Identify the blood parasite species.
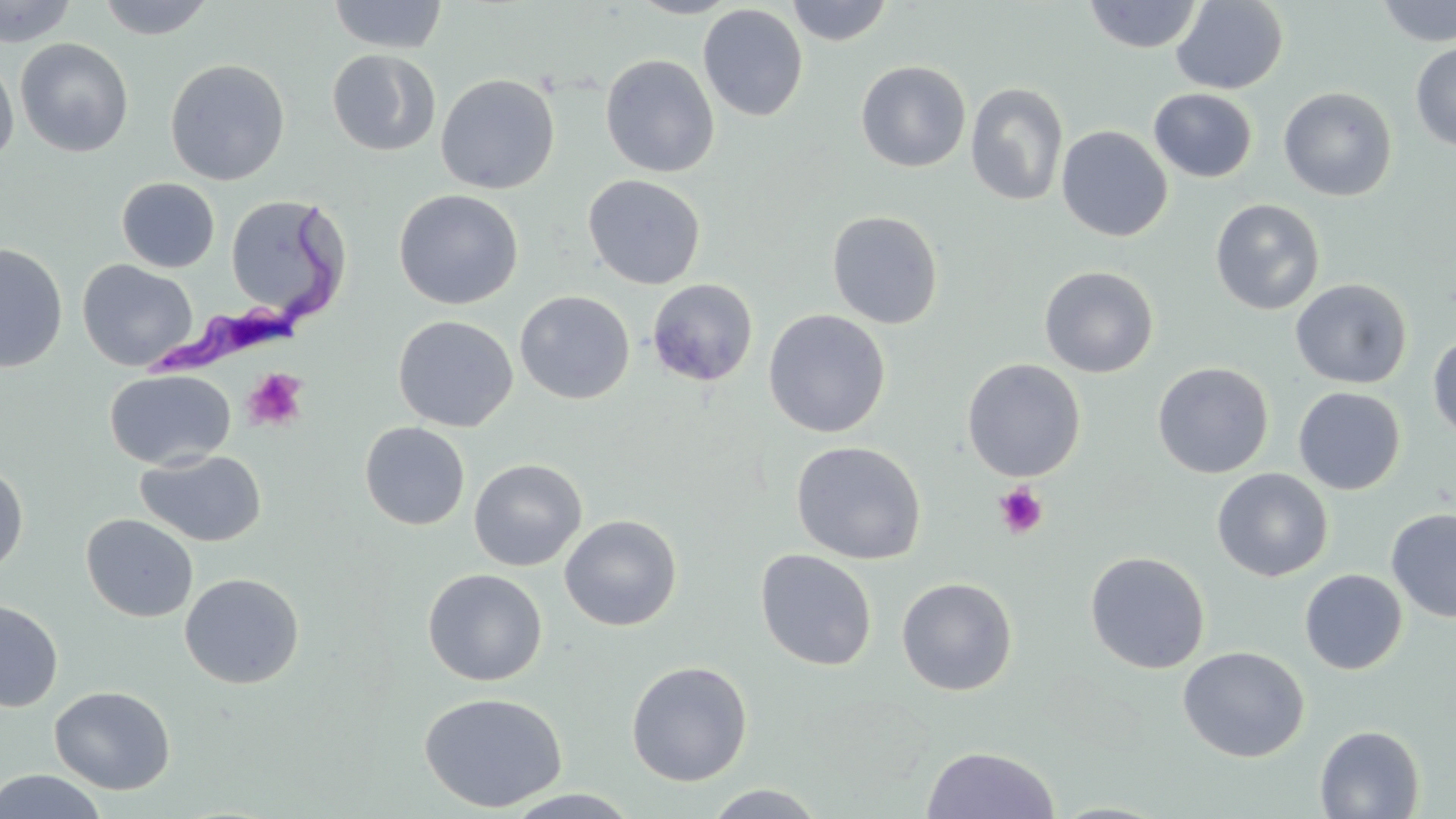
Trypanosoma brucei.

image size = 1456×819 pixels
platelet locations = approximate bounding boxes as named x1/y1/x2/y2 corners in pixels: (x1=241, y1=367, x2=309, y2=433), (x1=993, y1=483, x2=1049, y2=538)
stain = May-Grünwald-Giemsa
modality = optical microscopy
preparation = thin blood smear
magnification = 1000x
uninfected red blood cell locations = approximate bounding boxes as named x1/y1/x2/y2 corners in pixels: (x1=95, y1=0, x2=216, y2=40), (x1=328, y1=0, x2=448, y2=54), (x1=627, y1=0, x2=742, y2=19), (x1=785, y1=0, x2=894, y2=46), (x1=0, y1=1, x2=78, y2=47), (x1=1082, y1=1, x2=1204, y2=53), (x1=1170, y1=1, x2=1289, y2=94), (x1=1376, y1=1, x2=1456, y2=46), (x1=697, y1=4, x2=808, y2=122), (x1=16, y1=38, x2=134, y2=158), (x1=1410, y1=42, x2=1456, y2=153), (x1=326, y1=49, x2=441, y2=157), (x1=0, y1=52, x2=19, y2=165), (x1=600, y1=54, x2=720, y2=178), (x1=165, y1=58, x2=290, y2=186), (x1=856, y1=60, x2=971, y2=172), (x1=435, y1=73, x2=560, y2=194), (x1=965, y1=82, x2=1069, y2=207), (x1=1278, y1=86, x2=1397, y2=201), (x1=1149, y1=88, x2=1258, y2=183), (x1=1056, y1=125, x2=1173, y2=242), (x1=583, y1=174, x2=706, y2=289), (x1=116, y1=177, x2=220, y2=273), (x1=393, y1=189, x2=523, y2=309), (x1=225, y1=195, x2=349, y2=321), (x1=1210, y1=199, x2=1325, y2=315), (x1=826, y1=209, x2=944, y2=329), (x1=0, y1=242, x2=68, y2=373), (x1=77, y1=260, x2=198, y2=372), (x1=1039, y1=265, x2=1159, y2=378), (x1=1290, y1=278, x2=1412, y2=389), (x1=647, y1=279, x2=758, y2=387), (x1=515, y1=290, x2=635, y2=405), (x1=763, y1=309, x2=890, y2=438), (x1=393, y1=315, x2=518, y2=432), (x1=1427, y1=335, x2=1456, y2=442), (x1=961, y1=358, x2=1086, y2=482), (x1=1152, y1=362, x2=1274, y2=479), (x1=104, y1=369, x2=236, y2=469), (x1=1293, y1=387, x2=1406, y2=495), (x1=359, y1=422, x2=470, y2=531), (x1=790, y1=440, x2=926, y2=565), (x1=134, y1=449, x2=267, y2=548), (x1=468, y1=458, x2=587, y2=571), (x1=0, y1=460, x2=29, y2=577), (x1=1212, y1=467, x2=1333, y2=582), (x1=1386, y1=508, x2=1456, y2=623), (x1=81, y1=514, x2=198, y2=622), (x1=559, y1=514, x2=682, y2=631), (x1=755, y1=549, x2=877, y2=671), (x1=1085, y1=550, x2=1210, y2=674), (x1=423, y1=569, x2=547, y2=686), (x1=1299, y1=569, x2=1407, y2=675), (x1=179, y1=572, x2=304, y2=688), (x1=896, y1=576, x2=1018, y2=696), (x1=0, y1=599, x2=63, y2=712), (x1=1177, y1=646, x2=1309, y2=762), (x1=626, y1=660, x2=753, y2=786), (x1=49, y1=685, x2=175, y2=794), (x1=418, y1=691, x2=568, y2=813), (x1=1315, y1=724, x2=1425, y2=818), (x1=922, y1=746, x2=1060, y2=818), (x1=0, y1=769, x2=108, y2=819), (x1=703, y1=784, x2=827, y2=819), (x1=502, y1=789, x2=642, y2=818), (x1=1047, y1=802, x2=1171, y2=818)
field of view = one of a larger specimen
Trypanosoma brucei locations = approximate bounding boxes as named x1/y1/x2/y2 corners in pixels: (x1=142, y1=200, x2=336, y2=383)